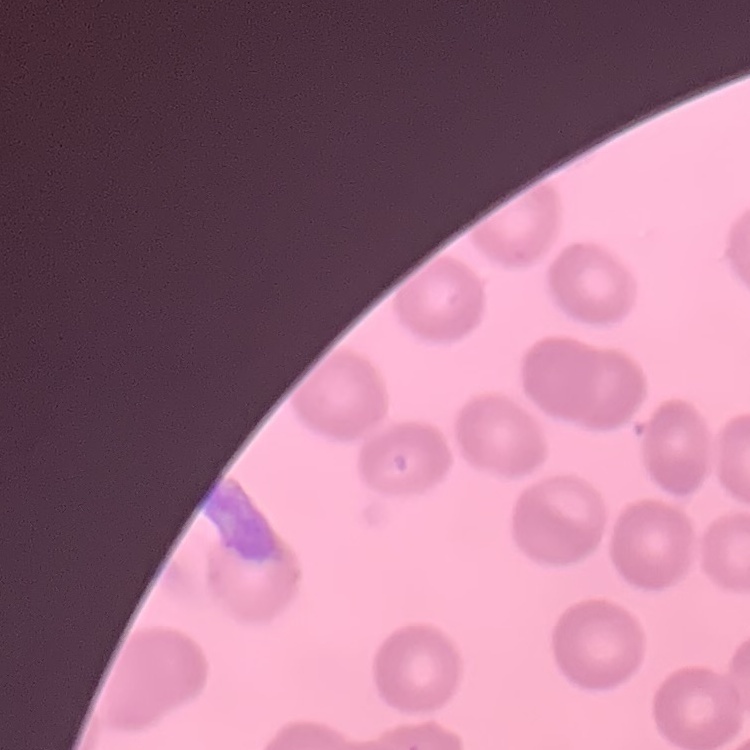

Summary:
  - Red blood cell morphology: no rouleaux formation
  - Stain: Field's or Giemsa
  - Preparation: thin peripheral smear
  - Image type: one tile cut from a larger photomicrograph